Assess this cell for malaria.
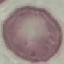

Uninfected.

Summary:
  - Preparation: thin blood film
  - Image type: automatically extracted cell patch, resized to 64 × 64 pixels
  - Capture: smartphone camera at the microscope eyepiece
  - Stain: Giemsa